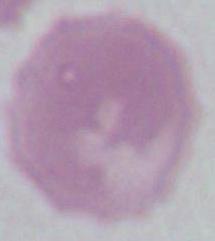

magnification: 1000x
identification: erythrocyte
modality: micrograph